Assess this cell for malaria.
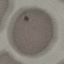

Uninfected.

preparation = thin smear
image type = cell patch, automatically extracted from a larger field of view and resized to 64 × 64 pixels
capture = smartphone through the microscope eyepiece
stain = Giemsa